Locate every leukocyte (white blood cell).
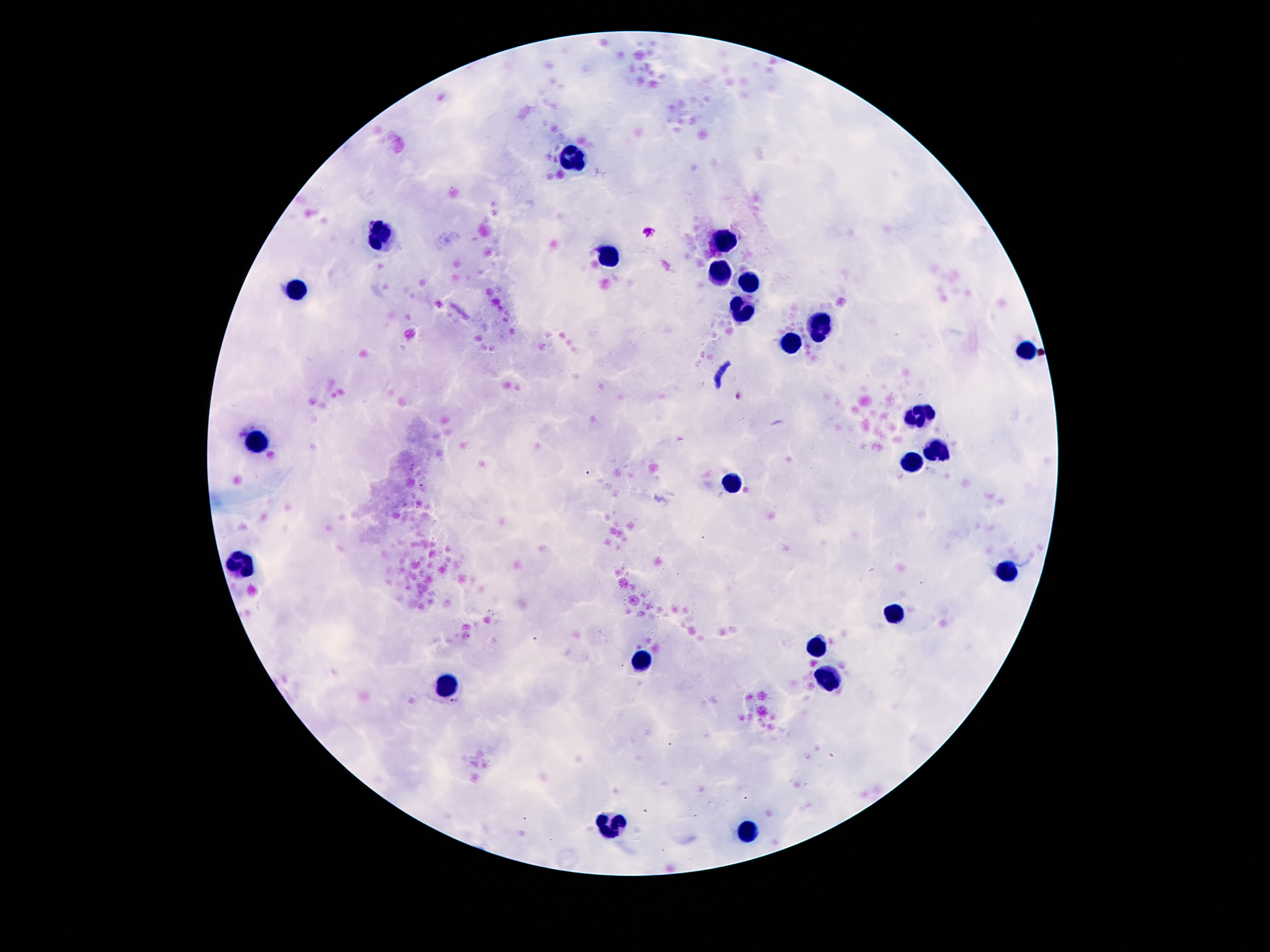
Approximate centers as {x, y} in pixels.
Leukocytes: {575, 157}, {384, 237}, {724, 243}, {608, 259}, {724, 271}, {747, 280}, {294, 286}, {741, 312}, {817, 327}, {792, 342}, {1026, 349}, {919, 415}, {257, 443}, {936, 448}, {913, 463}, {733, 485}, {241, 566}, {1009, 568}, {892, 613}, {817, 646}, {641, 659}, {827, 678}, {446, 685}, {610, 823}, {749, 829}.

{
  "magnification": "100x",
  "preparation": "thick peripheral-blood smear",
  "field_of_view": "single",
  "capture": "smartphone camera through the microscope eyepiece",
  "patient_malaria_status": "not infected",
  "image_size": "1270×952 pixels",
  "stain": "Giemsa"
}